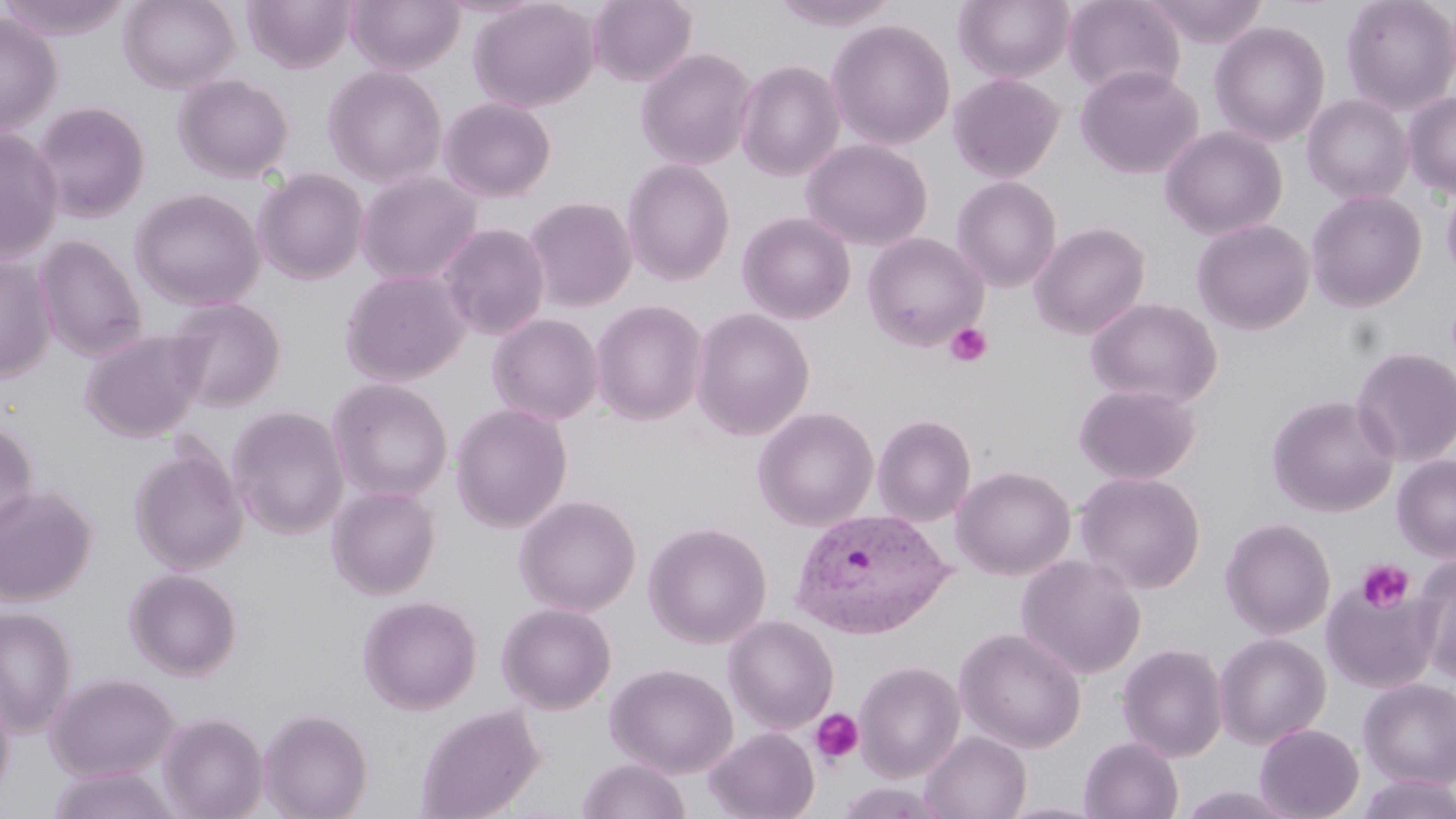
Approximate bounding boxes as named x1/y1/x2/y2 corners in pixels. Uninfected red blood cell locations: (x1=0, y1=0, x2=135, y2=40), (x1=117, y1=0, x2=239, y2=93), (x1=346, y1=0, x2=465, y2=75), (x1=469, y1=0, x2=599, y2=112), (x1=588, y1=0, x2=697, y2=86), (x1=769, y1=0, x2=902, y2=30), (x1=954, y1=0, x2=1075, y2=84), (x1=1062, y1=0, x2=1184, y2=99), (x1=1141, y1=0, x2=1270, y2=47), (x1=1340, y1=0, x2=1456, y2=114), (x1=243, y1=1, x2=356, y2=73), (x1=0, y1=13, x2=63, y2=137), (x1=827, y1=19, x2=956, y2=150), (x1=1209, y1=21, x2=1330, y2=146), (x1=636, y1=47, x2=758, y2=170), (x1=734, y1=60, x2=845, y2=181), (x1=322, y1=65, x2=448, y2=187), (x1=1076, y1=65, x2=1203, y2=179), (x1=948, y1=73, x2=1065, y2=182), (x1=173, y1=74, x2=294, y2=183), (x1=1402, y1=91, x2=1456, y2=198), (x1=1302, y1=94, x2=1414, y2=204), (x1=438, y1=97, x2=556, y2=201), (x1=32, y1=101, x2=151, y2=223), (x1=1159, y1=126, x2=1287, y2=240), (x1=0, y1=128, x2=64, y2=263), (x1=801, y1=139, x2=933, y2=251), (x1=622, y1=159, x2=735, y2=285), (x1=253, y1=168, x2=369, y2=285), (x1=356, y1=171, x2=482, y2=286), (x1=951, y1=176, x2=1062, y2=292), (x1=1441, y1=182, x2=1456, y2=283), (x1=129, y1=188, x2=266, y2=310), (x1=1306, y1=190, x2=1427, y2=312), (x1=524, y1=197, x2=637, y2=311), (x1=737, y1=212, x2=856, y2=324), (x1=1192, y1=219, x2=1315, y2=334), (x1=1030, y1=222, x2=1150, y2=338), (x1=437, y1=223, x2=550, y2=340), (x1=862, y1=233, x2=988, y2=350), (x1=32, y1=234, x2=146, y2=362), (x1=0, y1=255, x2=56, y2=382), (x1=340, y1=269, x2=470, y2=386), (x1=166, y1=297, x2=286, y2=412), (x1=1086, y1=297, x2=1223, y2=409), (x1=590, y1=300, x2=708, y2=425), (x1=691, y1=308, x2=814, y2=440), (x1=488, y1=314, x2=604, y2=425), (x1=79, y1=329, x2=207, y2=442), (x1=1350, y1=346, x2=1456, y2=467), (x1=327, y1=378, x2=453, y2=503), (x1=1073, y1=382, x2=1200, y2=484), (x1=1266, y1=394, x2=1399, y2=517), (x1=450, y1=404, x2=573, y2=532), (x1=227, y1=406, x2=350, y2=539), (x1=752, y1=407, x2=878, y2=531), (x1=872, y1=414, x2=976, y2=526), (x1=0, y1=420, x2=39, y2=539), (x1=129, y1=445, x2=248, y2=575), (x1=1392, y1=455, x2=1456, y2=562), (x1=951, y1=465, x2=1076, y2=580), (x1=1075, y1=472, x2=1205, y2=593), (x1=0, y1=485, x2=98, y2=606), (x1=327, y1=485, x2=441, y2=600), (x1=514, y1=495, x2=641, y2=616), (x1=1220, y1=517, x2=1336, y2=639), (x1=644, y1=522, x2=772, y2=648), (x1=1016, y1=554, x2=1147, y2=680), (x1=1413, y1=555, x2=1456, y2=683), (x1=124, y1=568, x2=243, y2=680), (x1=1321, y1=575, x2=1441, y2=694), (x1=358, y1=595, x2=482, y2=715), (x1=497, y1=602, x2=617, y2=714), (x1=0, y1=607, x2=77, y2=737), (x1=722, y1=615, x2=839, y2=734), (x1=954, y1=627, x2=1087, y2=753), (x1=1214, y1=632, x2=1331, y2=748), (x1=1116, y1=643, x2=1229, y2=761), (x1=854, y1=660, x2=964, y2=782), (x1=606, y1=663, x2=738, y2=778), (x1=45, y1=672, x2=179, y2=781), (x1=1358, y1=677, x2=1456, y2=788), (x1=0, y1=685, x2=15, y2=807), (x1=415, y1=704, x2=544, y2=819), (x1=258, y1=708, x2=373, y2=819), (x1=158, y1=712, x2=269, y2=819), (x1=1254, y1=723, x2=1364, y2=819), (x1=704, y1=727, x2=820, y2=819), (x1=920, y1=731, x2=1032, y2=818), (x1=1079, y1=736, x2=1184, y2=819), (x1=576, y1=758, x2=691, y2=819), (x1=46, y1=766, x2=183, y2=819), (x1=1354, y1=774, x2=1456, y2=819), (x1=835, y1=781, x2=949, y2=818). Plasmodium vivax-infected red blood cell locations: (x1=788, y1=506, x2=953, y2=639). Platelet locations: (x1=945, y1=323, x2=991, y2=367), (x1=1356, y1=559, x2=1413, y2=612), (x1=811, y1=708, x2=863, y2=765). Slide-level diagnosis: Plasmodium vivax. May-Grünwald-Giemsa stain. Thin blood smear. Image is 1456×819 pixels. Single field of view. Optical microscopy. 1000x magnification.